Name the cell type shown.
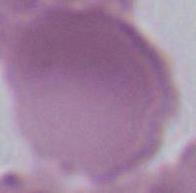
An erythrocyte.

Summary:
  - Magnification: 1000x
  - Modality: micrograph